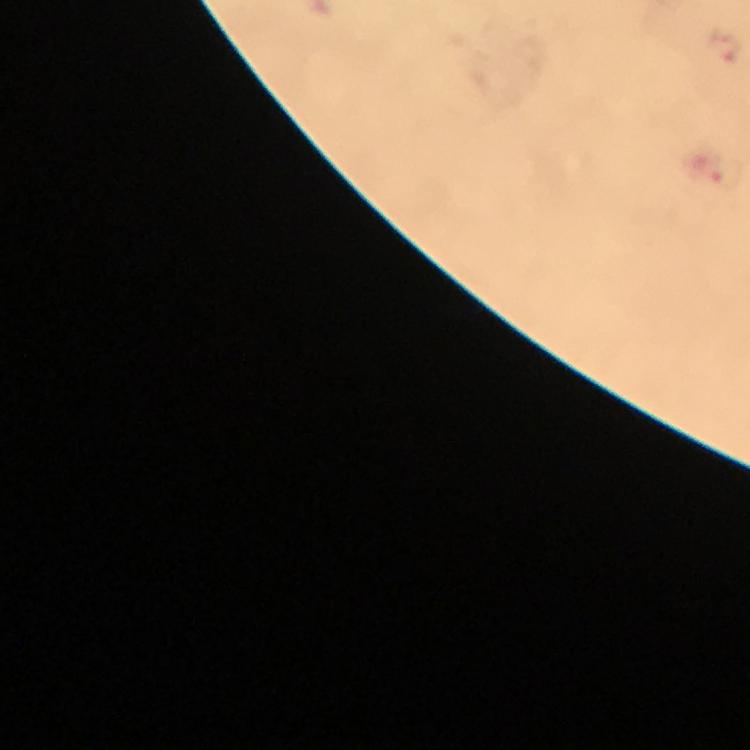 Approximate centers as (x, y) in pixels. Plasmodium parasite locations: (724, 47). A crop from one field of view. From a diagnostic examination for malaria. Image is 750×750 pixels. Thick blood film. Giemsa-stained preparation. At 100x magnification. Smartphone photograph taken through a microscope. Immersion oil was used.